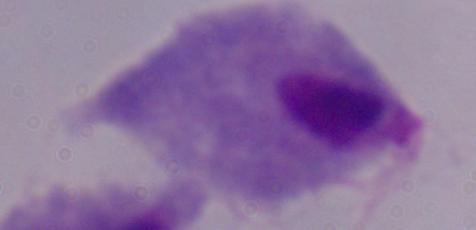
modality: micrograph
magnification: 1000x
identification: trichomonad